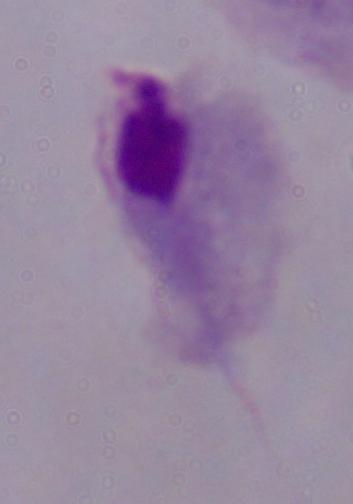
identification = trichomonad
modality = photomicrograph
magnification = 1000x